State which parasite is depicted.
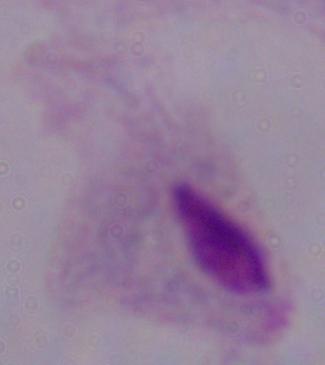

A trichomonad.

modality = micrograph
magnification = 1000x